Identify the preparation type.
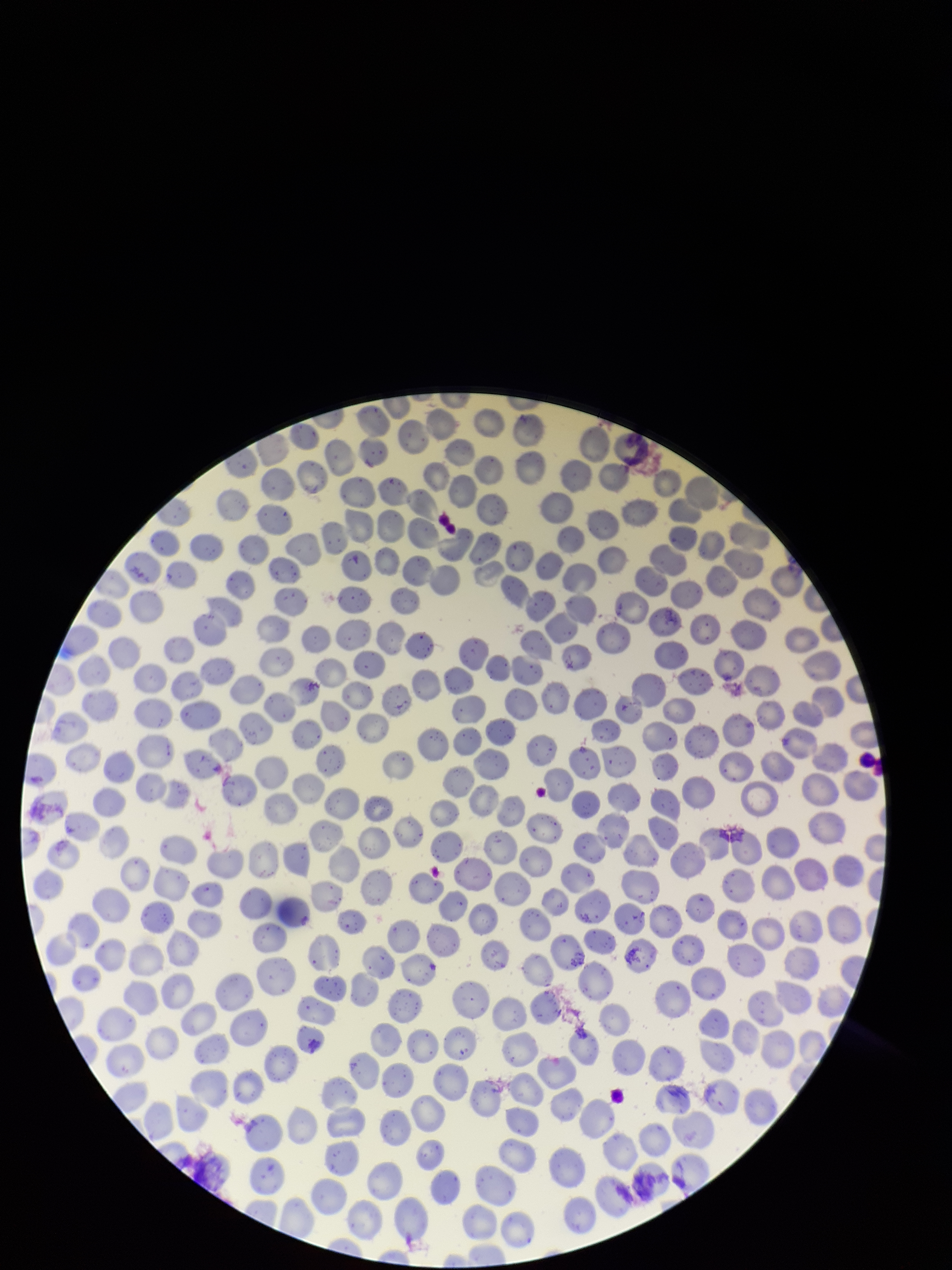
A thin smear.

Summary:
  - Red blood cell count: 316
  - Stain: Giemsa
  - Image size: 952×1270 pixels
  - Parasitized red blood cell count: 0
  - Patient malaria status: negative
  - Field of view: one from this slide
  - Capture: smartphone photograph through the microscope eyepiece
  - Parasitized red blood cells: none seen